Locate every Plasmodium ovale-infected red blood cell.
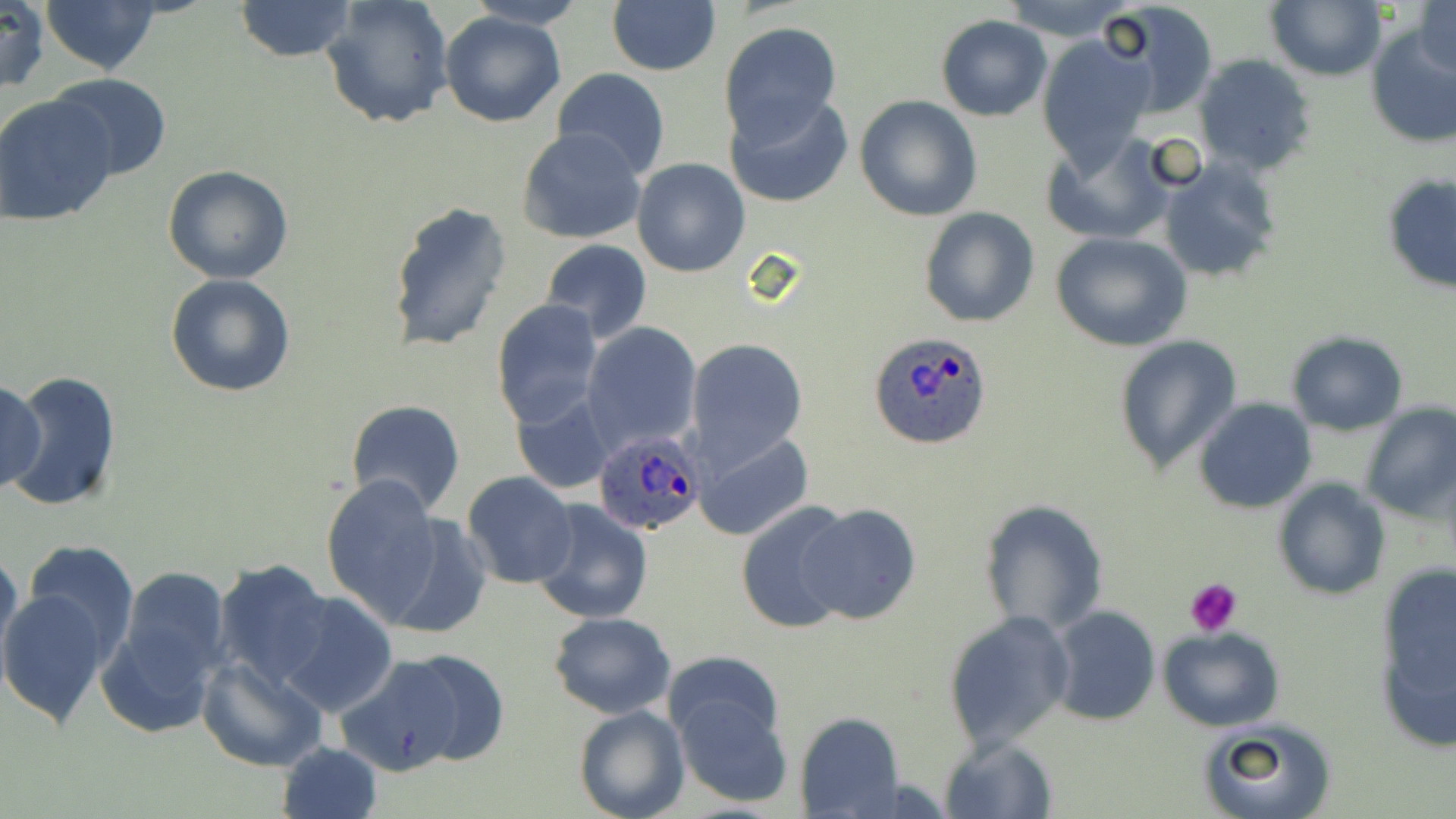
Approximate bounding boxes as named x1/y1/x2/y2 corners in pixels.
Plasmodium ovale-infected red blood cells: (x1=870, y1=332, x2=994, y2=450), (x1=591, y1=427, x2=704, y2=535).

slide-level diagnosis = Plasmodium ovale
preparation = thin blood film
platelet locations = approximate bounding boxes as named x1/y1/x2/y2 corners in pixels: (x1=1185, y1=577, x2=1244, y2=635)
stain = May-Grünwald-Giemsa
uninfected red blood cell locations = approximate bounding boxes as named x1/y1/x2/y2 corners in pixels: (x1=0, y1=0, x2=51, y2=95), (x1=39, y1=0, x2=162, y2=76), (x1=233, y1=0, x2=358, y2=62), (x1=320, y1=0, x2=455, y2=130), (x1=999, y1=0, x2=1135, y2=41), (x1=1097, y1=0, x2=1219, y2=118), (x1=1265, y1=0, x2=1385, y2=81), (x1=464, y1=1, x2=585, y2=29), (x1=608, y1=2, x2=721, y2=76), (x1=1415, y1=2, x2=1455, y2=80), (x1=440, y1=11, x2=568, y2=127), (x1=937, y1=16, x2=1052, y2=121), (x1=1363, y1=20, x2=1456, y2=150), (x1=720, y1=21, x2=842, y2=140), (x1=1037, y1=33, x2=1157, y2=169), (x1=1192, y1=54, x2=1317, y2=177), (x1=552, y1=67, x2=671, y2=179), (x1=48, y1=73, x2=173, y2=181), (x1=725, y1=92, x2=852, y2=209), (x1=0, y1=93, x2=120, y2=227), (x1=854, y1=95, x2=983, y2=223), (x1=517, y1=128, x2=648, y2=245), (x1=1043, y1=134, x2=1176, y2=246), (x1=1158, y1=157, x2=1282, y2=283), (x1=631, y1=158, x2=750, y2=278), (x1=162, y1=164, x2=294, y2=283), (x1=1382, y1=173, x2=1456, y2=294), (x1=387, y1=199, x2=513, y2=353), (x1=919, y1=207, x2=1040, y2=328), (x1=1050, y1=232, x2=1193, y2=352), (x1=539, y1=238, x2=652, y2=342), (x1=164, y1=273, x2=296, y2=398), (x1=493, y1=299, x2=604, y2=429), (x1=582, y1=322, x2=702, y2=451), (x1=1285, y1=332, x2=1409, y2=435), (x1=1112, y1=334, x2=1242, y2=476), (x1=687, y1=340, x2=809, y2=466), (x1=4, y1=370, x2=123, y2=512), (x1=0, y1=379, x2=46, y2=491), (x1=511, y1=391, x2=616, y2=495), (x1=345, y1=398, x2=467, y2=519), (x1=1194, y1=398, x2=1318, y2=514), (x1=1357, y1=401, x2=1455, y2=522), (x1=695, y1=431, x2=814, y2=542), (x1=462, y1=471, x2=577, y2=589), (x1=319, y1=473, x2=447, y2=621), (x1=1273, y1=479, x2=1391, y2=602), (x1=978, y1=498, x2=1108, y2=636), (x1=530, y1=500, x2=653, y2=624), (x1=736, y1=502, x2=856, y2=633), (x1=795, y1=504, x2=922, y2=625), (x1=376, y1=511, x2=492, y2=639), (x1=21, y1=539, x2=142, y2=665), (x1=0, y1=550, x2=26, y2=681), (x1=212, y1=559, x2=334, y2=689), (x1=115, y1=566, x2=233, y2=690), (x1=1371, y1=568, x2=1456, y2=751), (x1=0, y1=588, x2=111, y2=729), (x1=275, y1=591, x2=398, y2=716), (x1=1047, y1=605, x2=1161, y2=727), (x1=96, y1=608, x2=221, y2=741), (x1=942, y1=610, x2=1075, y2=753), (x1=547, y1=612, x2=676, y2=718), (x1=1158, y1=626, x2=1283, y2=731), (x1=664, y1=648, x2=782, y2=746), (x1=385, y1=649, x2=511, y2=767), (x1=337, y1=654, x2=470, y2=776), (x1=197, y1=655, x2=329, y2=771), (x1=672, y1=693, x2=794, y2=808), (x1=573, y1=705, x2=689, y2=819), (x1=795, y1=712, x2=904, y2=818), (x1=1196, y1=718, x2=1336, y2=819), (x1=939, y1=737, x2=1057, y2=819), (x1=275, y1=742, x2=384, y2=819)
modality = light microscopy
image size = 1456×819 pixels
magnification = 1000x
field of view = single